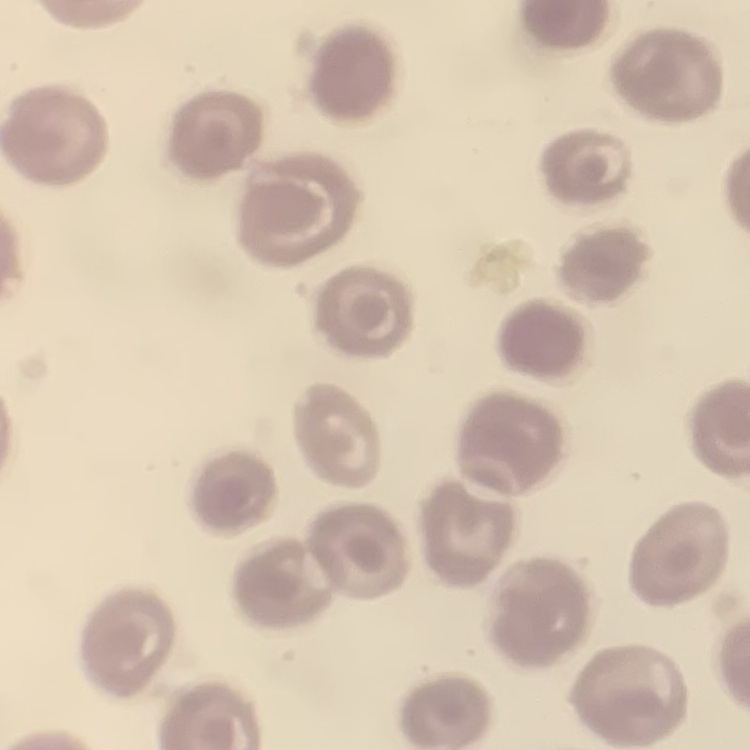
Summary:
  - Red blood cell morphology: no rouleaux formation
  - Stain: Field's or Giemsa
  - Image type: one tile cut from a larger photomicrograph
  - Preparation: thin blood smear